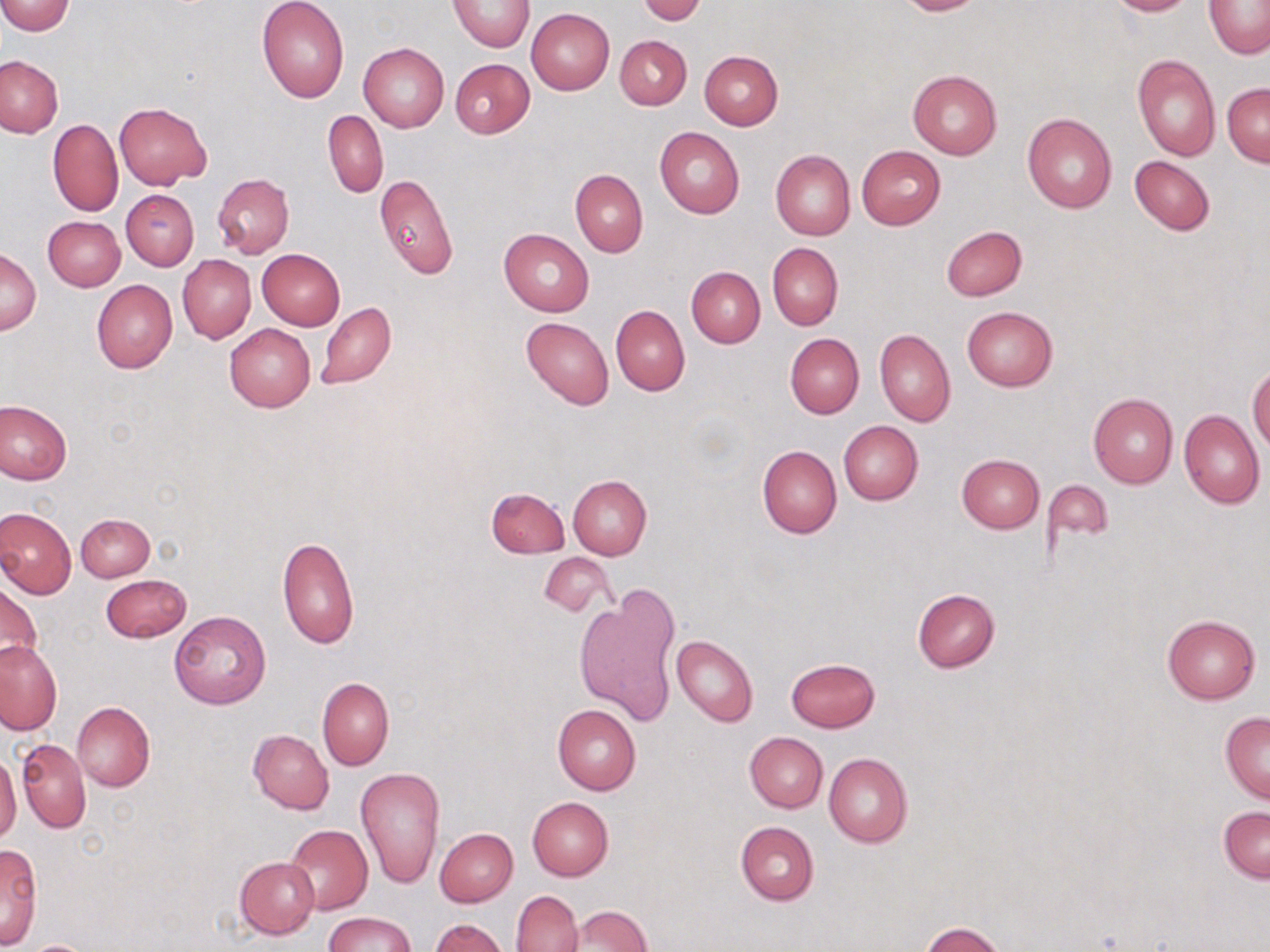

{
  "slide_level_diagnosis": "no evidence of blood parasites",
  "stain": "May-Grünwald-Giemsa",
  "field_of_view": "single",
  "preparation": "thin blood film",
  "magnification": "1000x",
  "image_size": "1270×952 pixels",
  "uninfected_red_blood_cell_locations": "approximate bounding boxes as named x1/y1/x2/y2 corners in pixels: (x1=448, y1=0, x2=535, y2=51), (x1=638, y1=0, x2=706, y2=24), (x1=893, y1=0, x2=988, y2=16), (x1=1104, y1=0, x2=1197, y2=16), (x1=0, y1=1, x2=75, y2=35), (x1=257, y1=1, x2=350, y2=102), (x1=1204, y1=1, x2=1270, y2=58), (x1=527, y1=9, x2=614, y2=94), (x1=616, y1=35, x2=692, y2=110), (x1=358, y1=42, x2=449, y2=132), (x1=699, y1=50, x2=783, y2=129), (x1=1131, y1=54, x2=1221, y2=161), (x1=1, y1=55, x2=63, y2=138), (x1=450, y1=58, x2=535, y2=137), (x1=907, y1=70, x2=1002, y2=160), (x1=1222, y1=83, x2=1270, y2=166), (x1=114, y1=102, x2=212, y2=189), (x1=322, y1=111, x2=388, y2=198), (x1=1022, y1=111, x2=1117, y2=214), (x1=48, y1=119, x2=123, y2=217), (x1=655, y1=126, x2=744, y2=218), (x1=856, y1=145, x2=945, y2=229), (x1=770, y1=149, x2=854, y2=241), (x1=1129, y1=155, x2=1214, y2=236), (x1=570, y1=169, x2=647, y2=256), (x1=211, y1=174, x2=294, y2=259), (x1=375, y1=174, x2=459, y2=279), (x1=121, y1=190, x2=199, y2=270), (x1=43, y1=215, x2=125, y2=291), (x1=941, y1=226, x2=1027, y2=301), (x1=499, y1=228, x2=594, y2=316), (x1=767, y1=243, x2=842, y2=330), (x1=1, y1=249, x2=40, y2=335), (x1=257, y1=249, x2=345, y2=330), (x1=178, y1=255, x2=256, y2=344), (x1=687, y1=266, x2=764, y2=347), (x1=91, y1=278, x2=178, y2=373), (x1=316, y1=302, x2=395, y2=390), (x1=611, y1=305, x2=689, y2=395), (x1=961, y1=306, x2=1058, y2=391), (x1=520, y1=316, x2=614, y2=409), (x1=225, y1=323, x2=315, y2=412), (x1=875, y1=329, x2=955, y2=426), (x1=784, y1=334, x2=864, y2=419), (x1=1248, y1=363, x2=1270, y2=453), (x1=1088, y1=393, x2=1178, y2=488), (x1=0, y1=401, x2=72, y2=484), (x1=1179, y1=409, x2=1265, y2=507), (x1=838, y1=421, x2=923, y2=505), (x1=757, y1=445, x2=841, y2=539), (x1=957, y1=454, x2=1045, y2=533), (x1=567, y1=474, x2=652, y2=559), (x1=1044, y1=480, x2=1114, y2=547), (x1=486, y1=486, x2=569, y2=559), (x1=0, y1=506, x2=77, y2=599), (x1=75, y1=513, x2=155, y2=581), (x1=277, y1=535, x2=360, y2=651), (x1=538, y1=553, x2=613, y2=618), (x1=101, y1=574, x2=191, y2=644), (x1=0, y1=581, x2=41, y2=672), (x1=912, y1=588, x2=1000, y2=672), (x1=575, y1=590, x2=679, y2=726), (x1=169, y1=611, x2=270, y2=710), (x1=1162, y1=615, x2=1260, y2=704), (x1=671, y1=635, x2=758, y2=726), (x1=0, y1=637, x2=61, y2=735), (x1=786, y1=657, x2=880, y2=732), (x1=318, y1=677, x2=394, y2=771), (x1=72, y1=701, x2=155, y2=791), (x1=552, y1=704, x2=642, y2=795), (x1=1220, y1=711, x2=1270, y2=802), (x1=248, y1=729, x2=334, y2=813), (x1=744, y1=732, x2=829, y2=812), (x1=17, y1=739, x2=92, y2=833), (x1=823, y1=752, x2=913, y2=847), (x1=0, y1=753, x2=21, y2=844), (x1=355, y1=767, x2=445, y2=888), (x1=528, y1=797, x2=613, y2=880), (x1=1218, y1=805, x2=1269, y2=883), (x1=736, y1=820, x2=819, y2=905), (x1=284, y1=824, x2=373, y2=915), (x1=435, y1=828, x2=518, y2=906), (x1=0, y1=843, x2=42, y2=947), (x1=234, y1=856, x2=319, y2=938), (x1=511, y1=890, x2=582, y2=952), (x1=565, y1=906, x2=651, y2=952), (x1=323, y1=912, x2=417, y2=952), (x1=429, y1=918, x2=507, y2=951), (x1=918, y1=922, x2=1008, y2=952), (x1=26, y1=940, x2=96, y2=952)",
  "modality": "optical microscopy"
}